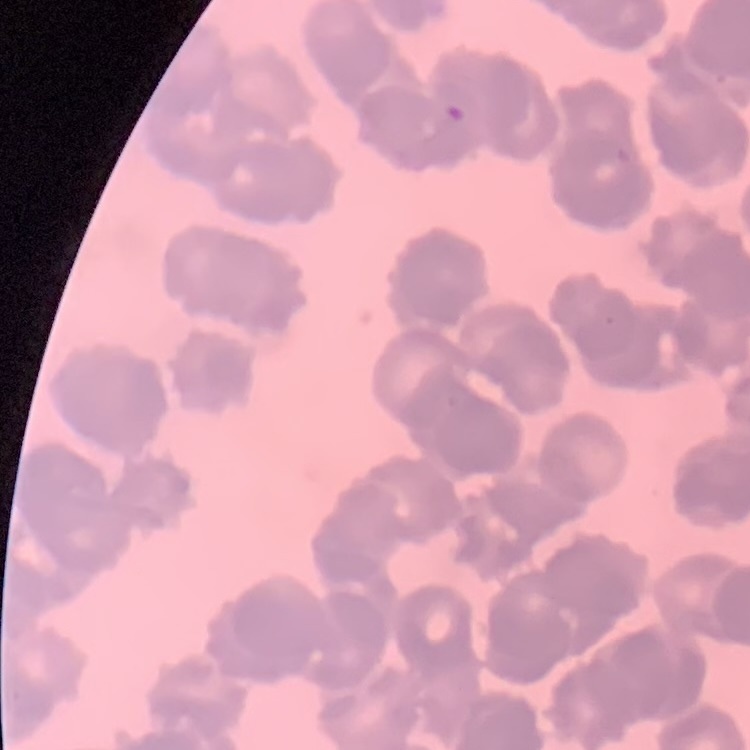
erythrocyte_morphology: rouleaux formation
preparation: thin blood smear
image_type: one tile cut from a larger photomicrograph
stain: Field's or Giemsa